Locate every Plasmodium parasite and every leukocyte.
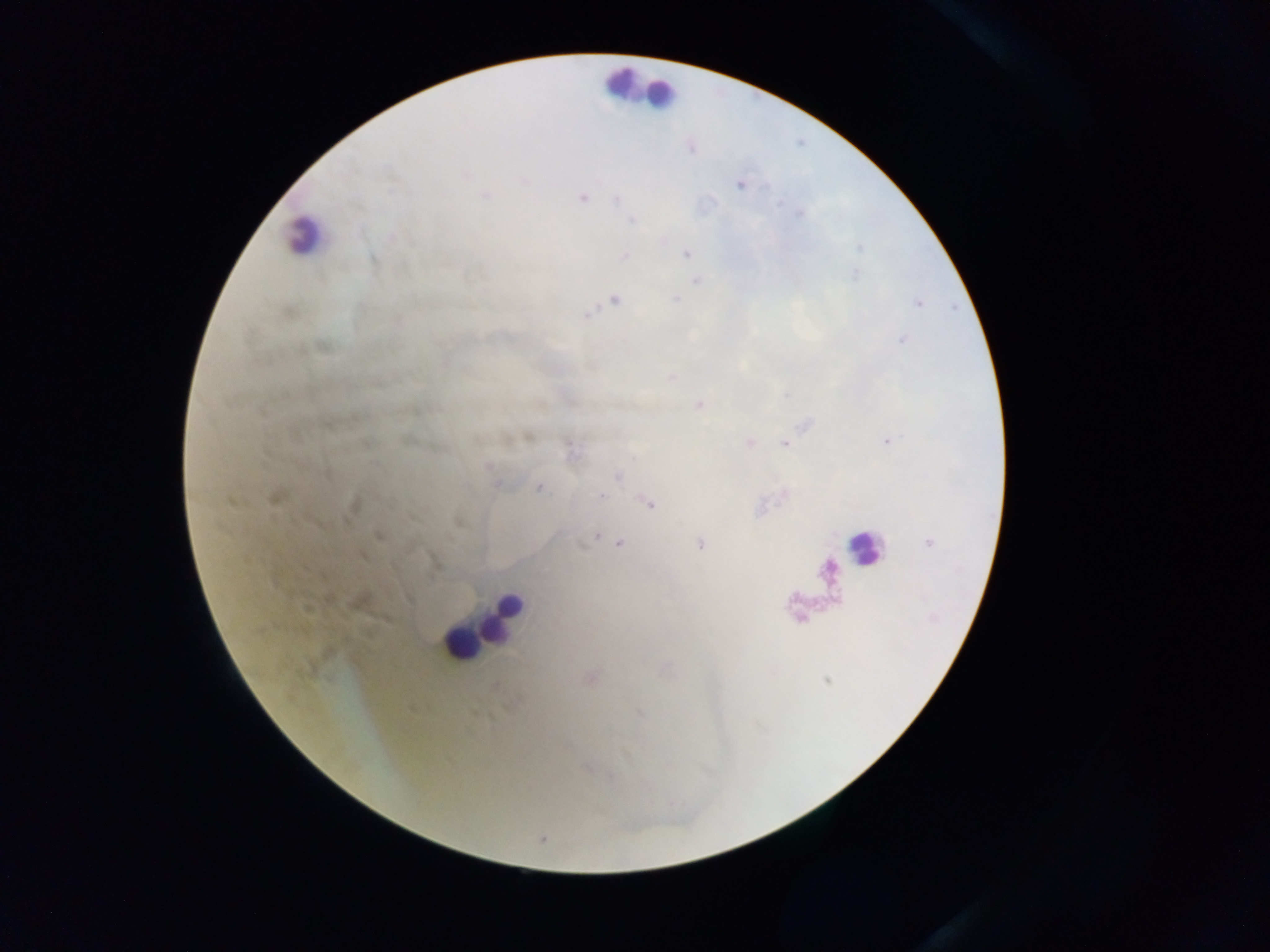
Approximate centers as x y in pixels.
Plasmodium parasites: 467 175; 525 181; 740 185; 390 190; 486 196; 582 198; 617 199; 632 221; 392 238; 686 254; 625 255; 373 258; 695 281; 677 299; 615 300; 587 314; 322 349; 699 405; 887 442; 750 443; 784 443; 617 476; 539 487; 601 496; 276 498; 649 504; 596 535; 378 536; 620 543; 700 544; 306 608.
Leukocytes: 624 83; 660 94; 304 234; 862 547; 503 615; 461 644.

image_size: 1270×952 pixels
preparation: thick blood smear
field_of_view: single
country: Ghana
capture: mobile-phone photograph through a microscope